Report the malaria status of this cell.
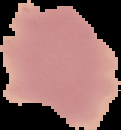

Uninfected.

The area outside the segmented cell region is set to black. Image is 121×130 pixels. From a thin blood smear.